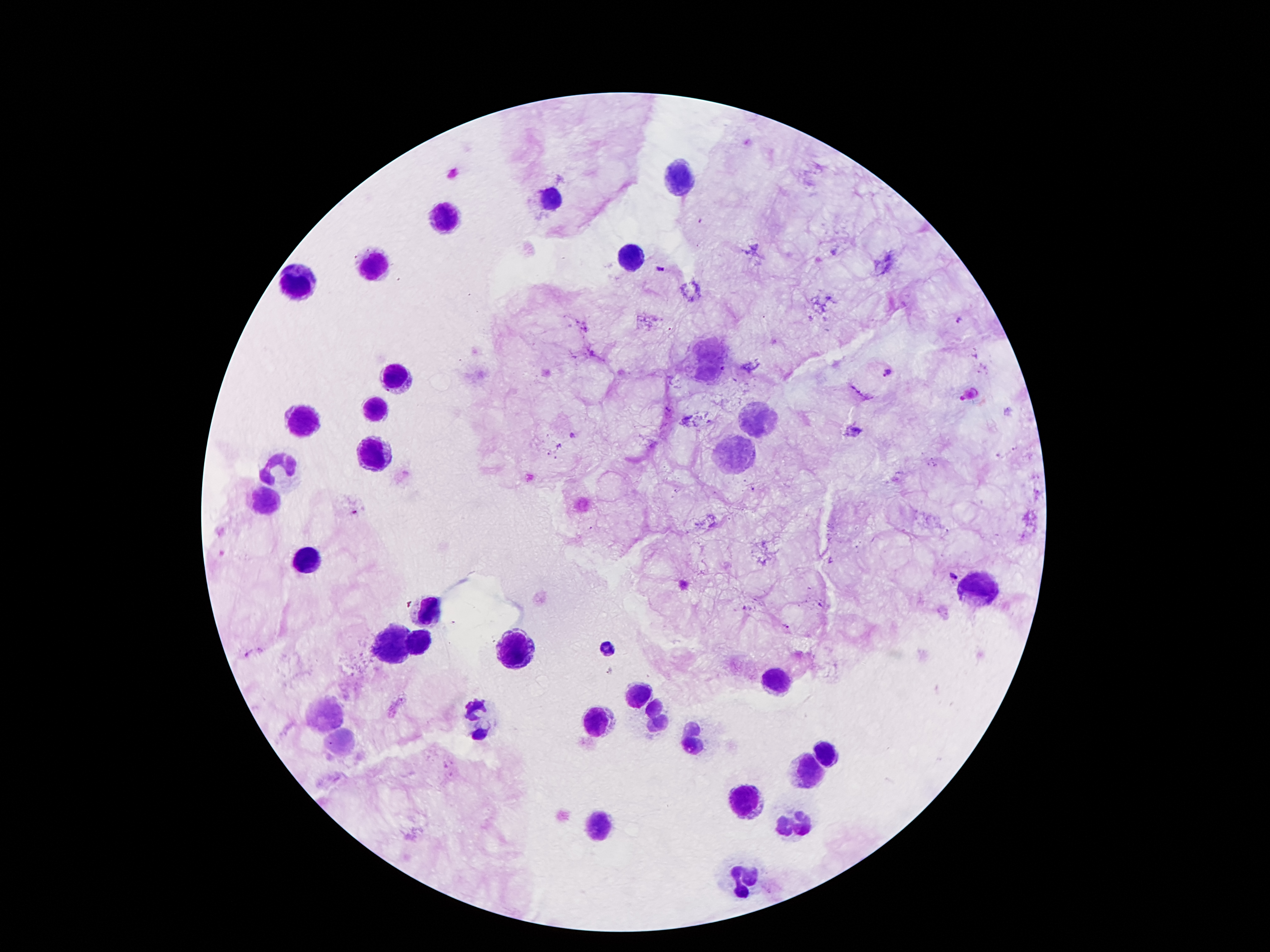

coordinate format = approximate centers as [x, y] in pixels
leukocyte locations = [680, 177], [552, 197], [444, 217], [632, 256], [375, 267], [298, 285], [704, 358], [394, 377], [375, 408], [303, 420], [752, 420], [736, 449], [375, 454], [280, 469], [269, 501], [305, 561], [977, 586], [426, 608], [393, 640], [418, 642], [512, 649], [604, 650], [782, 678], [641, 694], [326, 713], [603, 717], [654, 717], [477, 720], [696, 736], [339, 738], [830, 756], [813, 770], [750, 801], [602, 820], [795, 822], [746, 878]
Plasmodium parasite locations = [663, 269], [961, 318], [889, 372], [358, 513], [952, 576], [783, 626], [245, 654], [610, 670]
preparation = thick blood film
field of view = one from this slide
magnification = 100x
patient malaria status = positive for Plasmodium falciparum
image size = 1270×952 pixels
stain = Giemsa
capture = smartphone through the microscope eyepiece